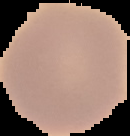

Summary:
  - Image size: 130×136 pixels
  - Malaria status: uninfected
  - Image type: segmented cell region on a black background
  - Preparation: thin blood smear